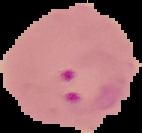 From a thin blood film. Image is 142×133 pixels. Segmented cell region on a black background. Result: malaria parasites identified.